Report the malaria status of this cell.
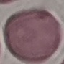

It is uninfected.

Cell patch, automatically extracted from a larger field of view and resized to 64 × 64 pixels. Thin blood smear. Acquired by smartphone through the microscope eyepiece. Giemsa-stained preparation.